State the preparation type.
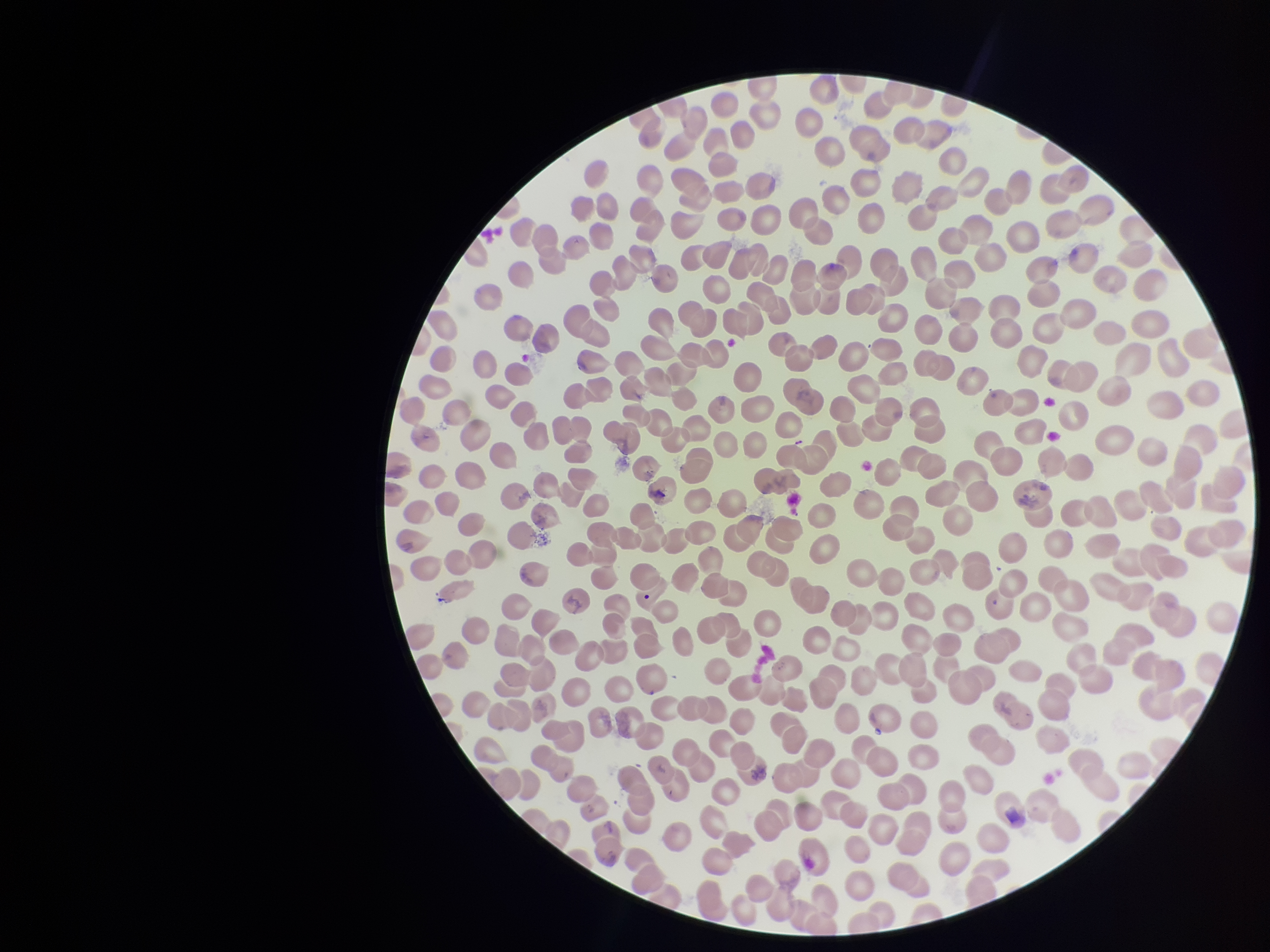

It is a thin blood smear.

Smartphone photograph taken through the eyepiece of a microscope. Parasitized red blood cells: none seen. Image is 1270×952 pixels. Patient malaria status: negative. Parasitized red blood cell count: 0. Giemsa stain. One field from this slide. Red blood cell count: 387.